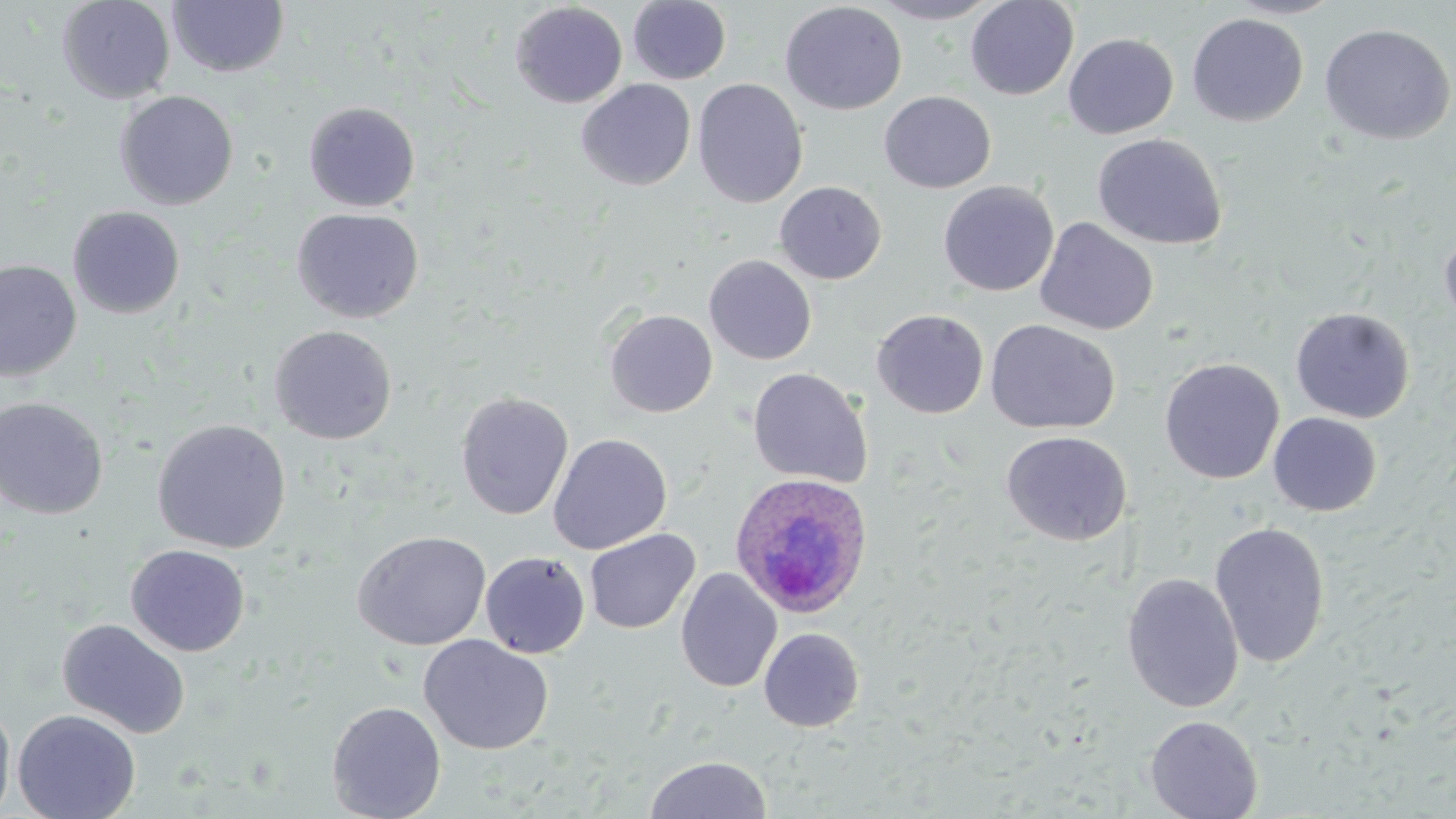
Summary:
  - Coordinate format: approximate bounding boxes as named x1/y1/x2/y2 corners in pixels
  - Uninfected red blood cell locations: (x1=57, y1=0, x2=175, y2=104), (x1=965, y1=0, x2=1079, y2=100), (x1=1223, y1=0, x2=1344, y2=19), (x1=167, y1=1, x2=290, y2=78), (x1=627, y1=1, x2=731, y2=85), (x1=780, y1=1, x2=907, y2=115), (x1=869, y1=1, x2=1002, y2=24), (x1=510, y1=2, x2=628, y2=108), (x1=1187, y1=13, x2=1308, y2=127), (x1=1319, y1=23, x2=1455, y2=145), (x1=1063, y1=33, x2=1179, y2=138), (x1=693, y1=78, x2=808, y2=209), (x1=576, y1=79, x2=696, y2=191), (x1=115, y1=90, x2=239, y2=210), (x1=879, y1=91, x2=996, y2=193), (x1=303, y1=101, x2=420, y2=212), (x1=1092, y1=133, x2=1228, y2=251), (x1=774, y1=181, x2=886, y2=284), (x1=938, y1=181, x2=1059, y2=297), (x1=67, y1=205, x2=185, y2=319), (x1=291, y1=207, x2=424, y2=323), (x1=1034, y1=217, x2=1159, y2=336), (x1=1439, y1=225, x2=1456, y2=337), (x1=703, y1=255, x2=817, y2=365), (x1=0, y1=260, x2=82, y2=383), (x1=1291, y1=307, x2=1415, y2=423), (x1=604, y1=309, x2=718, y2=418), (x1=872, y1=309, x2=989, y2=419), (x1=985, y1=319, x2=1120, y2=434), (x1=268, y1=325, x2=397, y2=445), (x1=1159, y1=357, x2=1284, y2=484), (x1=747, y1=368, x2=873, y2=488), (x1=456, y1=391, x2=574, y2=520), (x1=0, y1=397, x2=108, y2=520), (x1=1268, y1=412, x2=1382, y2=516), (x1=151, y1=419, x2=291, y2=553), (x1=1001, y1=430, x2=1132, y2=546), (x1=548, y1=433, x2=672, y2=554), (x1=1209, y1=522, x2=1330, y2=668), (x1=585, y1=529, x2=700, y2=634), (x1=352, y1=531, x2=491, y2=651), (x1=126, y1=544, x2=251, y2=656), (x1=480, y1=552, x2=590, y2=658), (x1=675, y1=568, x2=782, y2=693), (x1=1121, y1=573, x2=1244, y2=713), (x1=56, y1=618, x2=191, y2=738), (x1=759, y1=627, x2=865, y2=732), (x1=418, y1=634, x2=554, y2=755), (x1=0, y1=699, x2=16, y2=818), (x1=326, y1=700, x2=446, y2=819), (x1=12, y1=709, x2=141, y2=819), (x1=1144, y1=715, x2=1263, y2=819), (x1=645, y1=755, x2=771, y2=818)
  - Plasmodium ovale-infected red blood cell locations: (x1=729, y1=472, x2=874, y2=619)
  - Slide-level diagnosis: Plasmodium ovale
  - Field of view: single
  - Modality: light microscopy
  - Preparation: thin blood smear
  - Image size: 1456×819 pixels
  - Magnification: 1000x
  - Stain: May-Grünwald-Giemsa